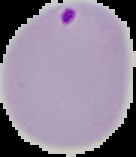
{
  "image_size": "136×157 pixels",
  "image_type": "segmented cell region on a black background",
  "preparation": "thin blood film",
  "malaria_status": "parasitized"
}